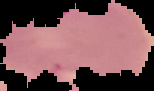

image size = 154×91 pixels
malaria status = parasitized
preparation = thin blood smear
image type = cell region segmented out of the field of view; surrounding area masked to black